Outline each uninfected red blood cell.
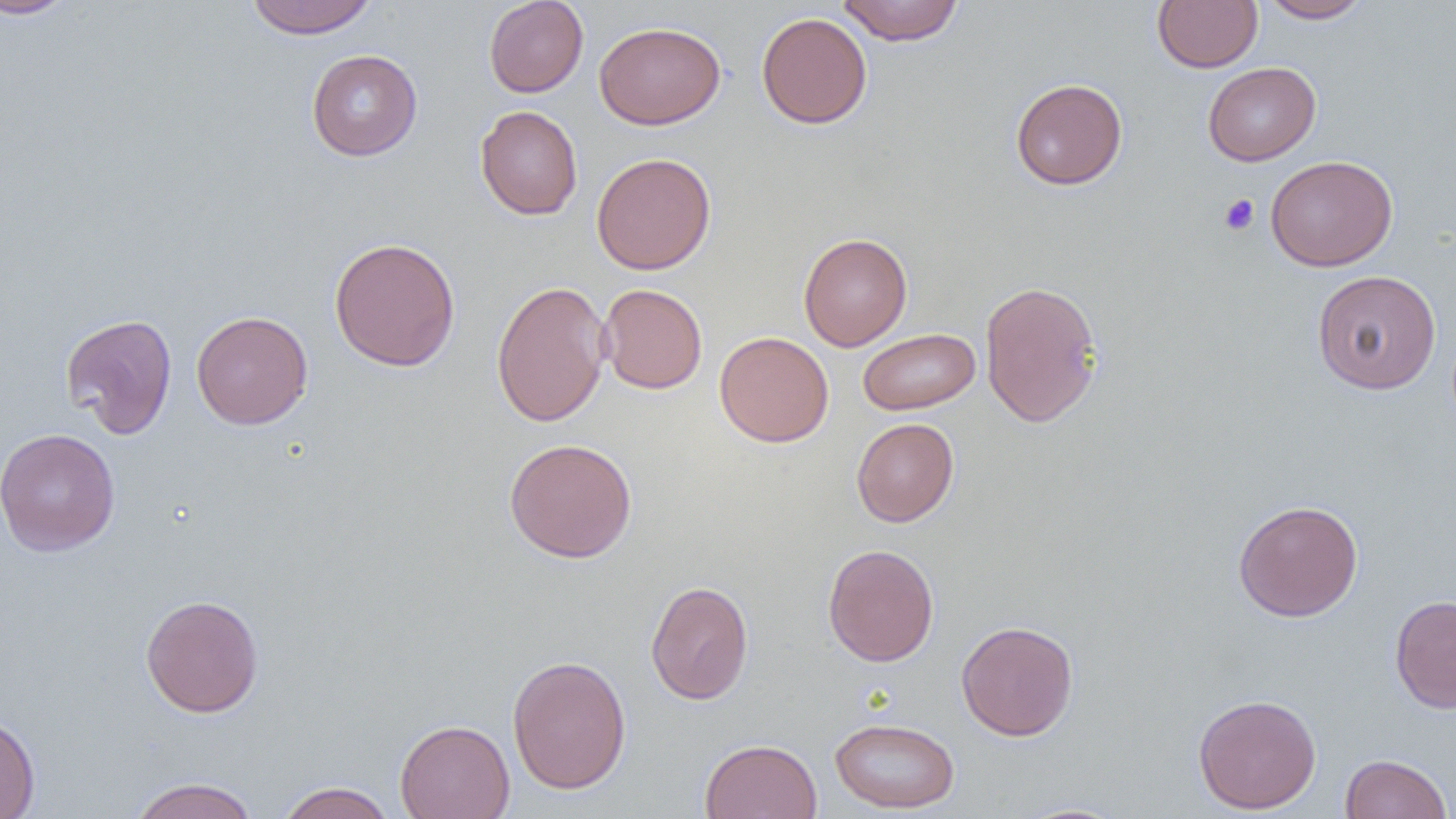
Approximate bounding boxes as (x1,y1)-(x2,y2) corner pairs in pixels.
Uninfected red blood cells: (0,0)-(80,20), (244,0)-(378,38), (483,0)-(589,97), (836,0)-(964,45), (1152,0)-(1263,73), (1258,0)-(1373,23), (756,12)-(872,129), (594,20)-(725,130), (306,49)-(422,161), (1203,62)-(1321,165), (1010,78)-(1128,190), (475,104)-(583,220), (591,151)-(716,275), (1265,155)-(1397,271), (798,232)-(912,350), (329,237)-(461,371), (1312,270)-(1442,394), (979,279)-(1104,428), (491,280)-(611,427), (597,283)-(708,394), (191,310)-(313,430), (60,313)-(178,438), (857,328)-(980,415), (714,331)-(834,447), (851,418)-(959,527), (1,427)-(120,557), (504,438)-(638,563), (1233,499)-(1363,622), (823,543)-(939,667), (645,580)-(754,705), (140,593)-(264,718), (1389,593)-(1456,714), (956,620)-(1078,741), (506,654)-(632,795), (1192,693)-(1322,815), (0,713)-(40,819), (830,717)-(960,813), (395,718)-(515,819), (699,738)-(822,819), (1341,753)-(1452,819), (127,777)-(260,819), (275,781)-(396,819), (1012,801)-(1132,818).

Platelet locations: (1219,193)-(1259,235). Slide-level diagnosis: no evidence of blood parasites. Image is 1456×819 pixels. Optical microscopy. 1000x magnification. Single field of view. Thin blood film.